Classify this cell by malaria status.
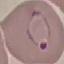

It is parasitized.

Thin blood film. Photographed with a smartphone camera at the microscope eyepiece. Giemsa-stained preparation. Automatically extracted cell patch, resized to 64 × 64 pixels.